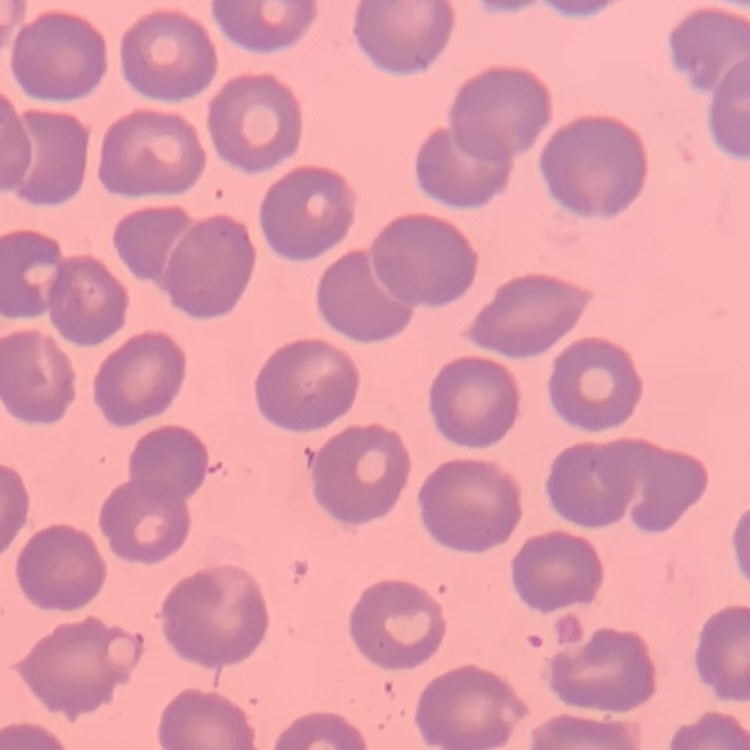

Summary:
  - Erythrocyte morphology: no rouleaux formation
  - Stain: Field's or Giemsa
  - Preparation: thin peripheral smear
  - Image type: square crop of a larger photomicrograph